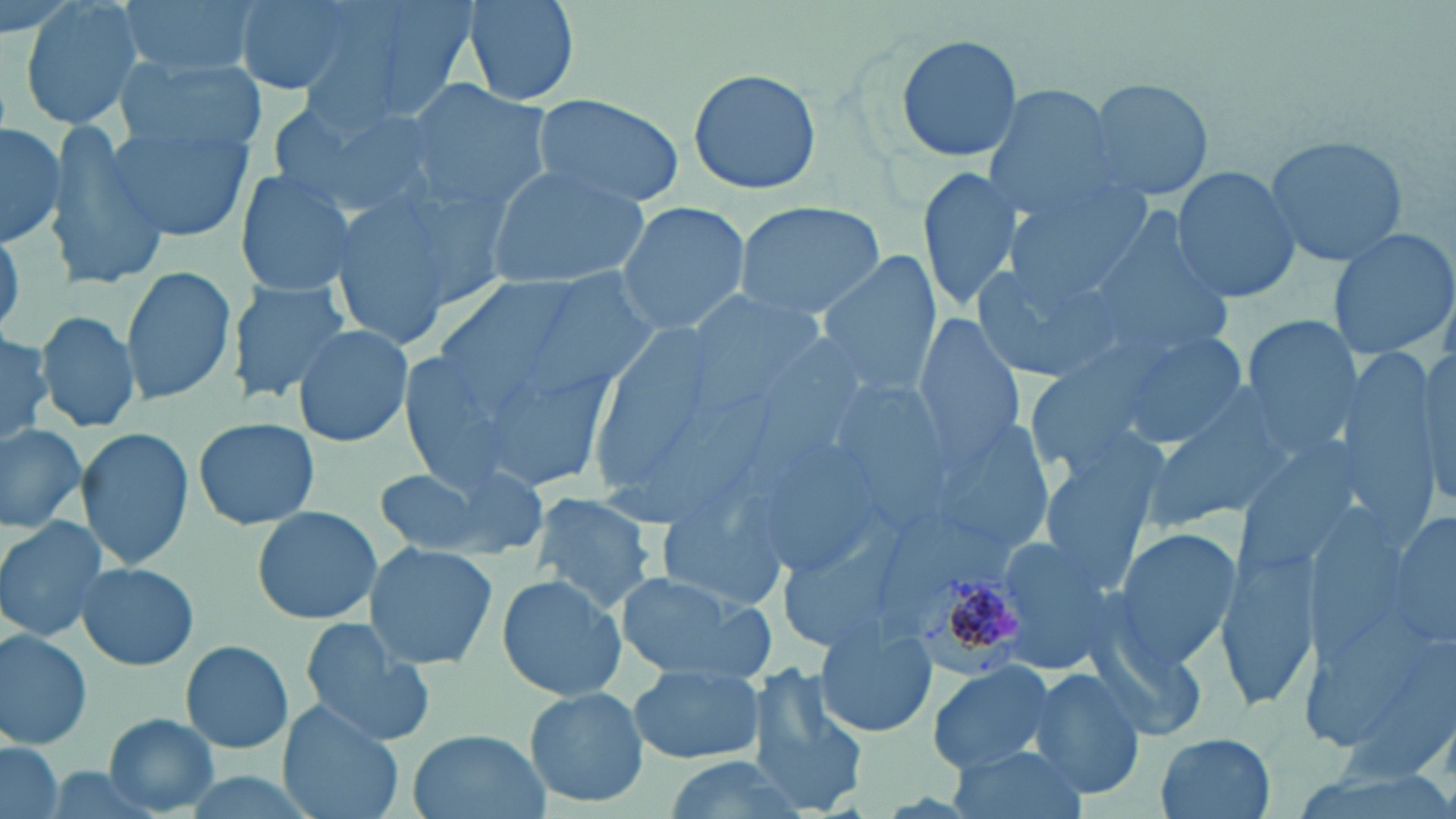

Summary:
  - Coordinate format: approximate bounding boxes as [x1, y1, x2, y2] in pixels
  - Uninfected red blood cell locations: [18, 0, 148, 133], [121, 0, 261, 76], [233, 0, 371, 97], [297, 0, 473, 129], [459, 0, 580, 108], [895, 31, 1023, 163], [121, 54, 268, 160], [688, 66, 822, 196], [1086, 76, 1215, 205], [400, 77, 552, 212], [978, 82, 1128, 219], [531, 94, 688, 207], [45, 117, 166, 293], [105, 118, 255, 243], [0, 121, 65, 245], [1265, 132, 1410, 266], [1169, 164, 1302, 303], [485, 165, 650, 290], [916, 165, 1025, 314], [234, 169, 362, 297], [1007, 181, 1153, 296], [323, 191, 462, 348], [613, 199, 753, 338], [731, 200, 885, 318], [1080, 209, 1236, 360], [0, 224, 23, 338], [1325, 225, 1456, 362], [816, 251, 943, 397], [968, 257, 1119, 383], [119, 265, 236, 405], [429, 271, 636, 409], [223, 280, 351, 405], [685, 287, 821, 404], [36, 310, 140, 434], [911, 314, 1027, 459], [1238, 315, 1364, 456], [584, 323, 748, 514], [293, 324, 413, 448], [1115, 327, 1250, 448], [0, 332, 52, 446], [1416, 339, 1456, 516], [1332, 344, 1445, 530], [395, 347, 527, 484], [470, 357, 610, 493], [1021, 360, 1163, 480], [825, 378, 948, 504], [1139, 383, 1292, 532], [919, 413, 1059, 560], [192, 417, 318, 530], [0, 423, 86, 533], [77, 426, 193, 570], [1232, 431, 1372, 580], [1035, 438, 1167, 591], [372, 464, 539, 565], [528, 489, 661, 611], [657, 492, 793, 608], [250, 504, 382, 626], [1374, 504, 1456, 654], [0, 516, 110, 642], [1110, 526, 1241, 665], [991, 533, 1125, 668], [363, 541, 498, 670], [1219, 549, 1318, 711], [75, 561, 199, 671], [613, 571, 775, 686], [496, 574, 625, 701], [1081, 613, 1209, 739], [298, 619, 437, 746], [816, 628, 937, 739], [0, 629, 93, 751], [181, 640, 295, 754], [924, 661, 1059, 774], [628, 665, 764, 767], [1023, 666, 1147, 800], [746, 667, 870, 818], [524, 687, 651, 810], [278, 699, 403, 819], [103, 713, 221, 815], [405, 728, 547, 819], [1152, 733, 1278, 819], [0, 742, 62, 819], [946, 747, 1090, 819], [664, 759, 807, 819], [1283, 762, 1456, 819]
  - Plasmodium malariae-infected red blood cell locations: [915, 572, 1026, 680]
  - Slide-level diagnosis: Plasmodium malariae
  - Field of view: one of a larger specimen
  - Image size: 1456×819 pixels
  - Magnification: 1000x
  - Modality: light microscopy
  - Stain: May-Grünwald-Giemsa
  - Preparation: thin blood smear